Name the cell type shown.
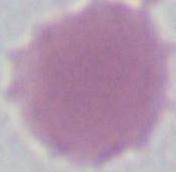

This is an erythrocyte.

magnification = 1000x
modality = photomicrograph